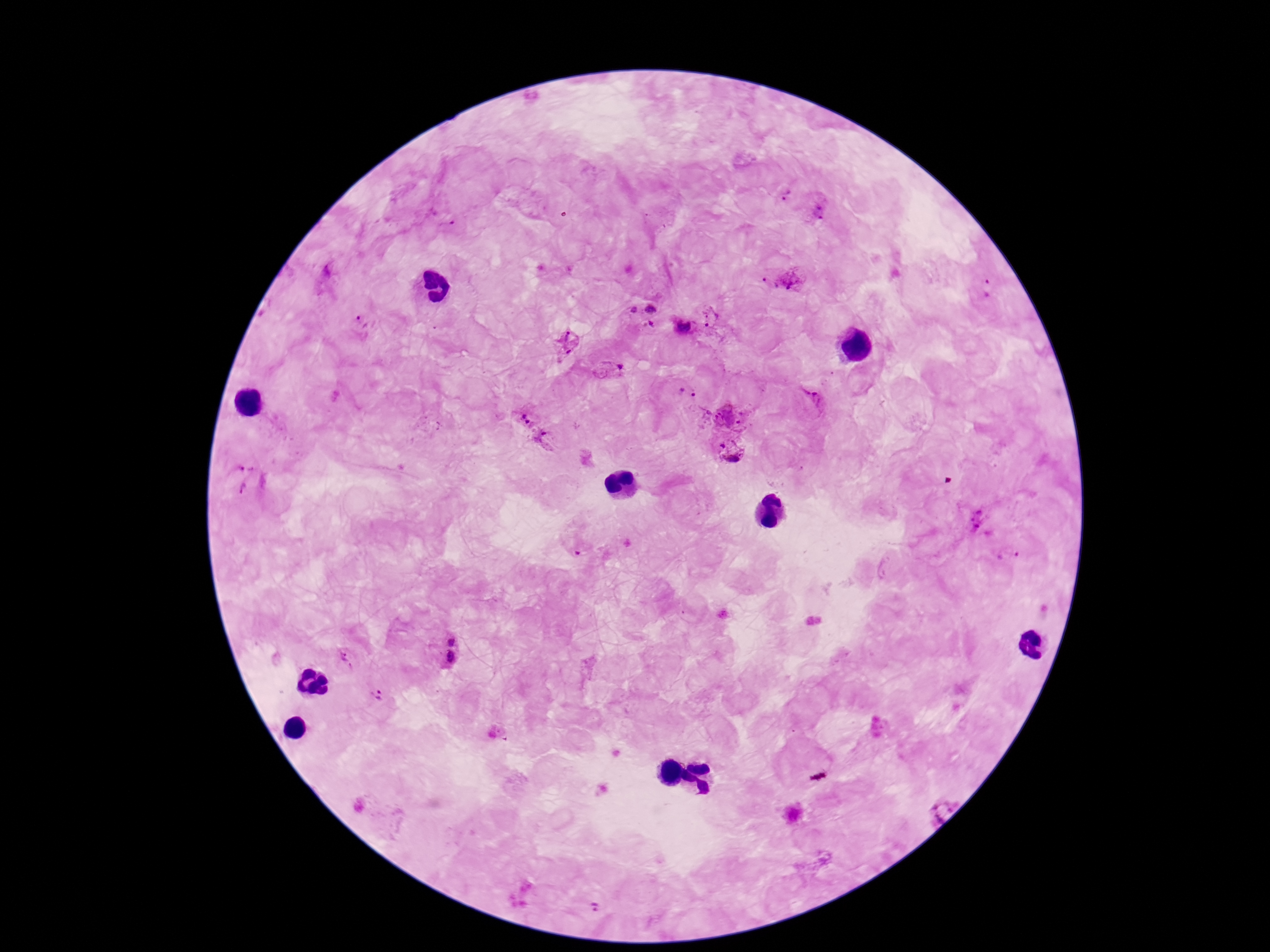
field of view = single
magnification = 100x
capture = smartphone camera through the microscope eyepiece
image size = 1270×952 pixels
Plasmodium parasite locations = approximate centers as (x, y) in pixels: (788, 196), (817, 213), (453, 231), (794, 278), (766, 285), (991, 288), (634, 311), (651, 311), (712, 319), (365, 325), (685, 327), (649, 329), (565, 338), (609, 367), (684, 395), (812, 402), (729, 412), (526, 416), (550, 443), (729, 452), (250, 464), (245, 487), (980, 518), (1008, 556), (450, 636), (449, 656), (347, 661), (376, 696), (938, 808), (597, 906)
patient malaria status = positive
preparation = thick peripheral-blood smear
stain = Giemsa